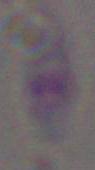
Summary:
  - Identification: Toxoplasma gondii
  - Magnification: 1000x
  - Modality: photomicrograph